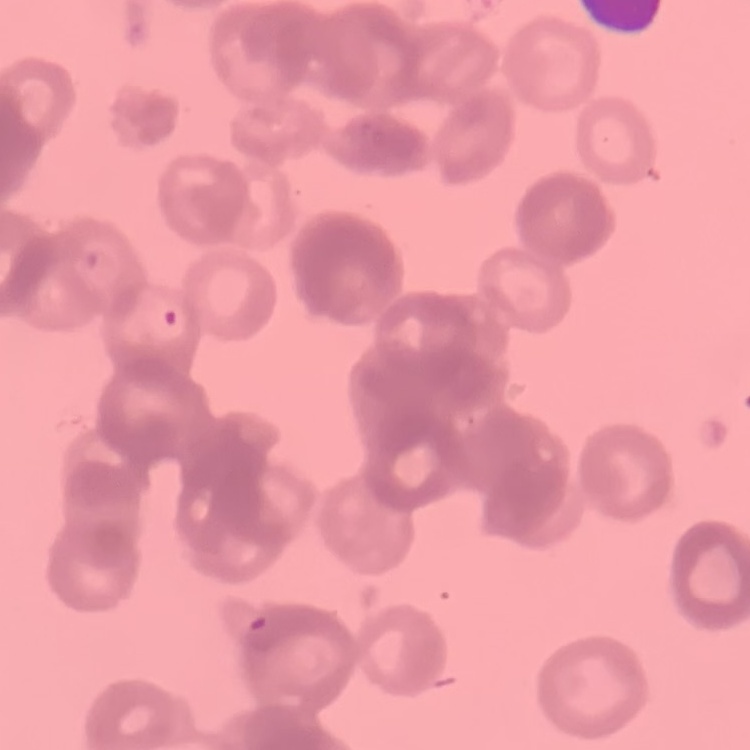

Summary:
  - Erythrocyte morphology: rouleaux formation
  - Stain: Field's or Giemsa
  - Preparation: thin blood smear
  - Image type: square crop of a larger photomicrograph